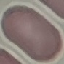
Summary:
  - Malaria status: uninfected
  - Stain: Giemsa
  - Preparation: thin smear
  - Capture: smartphone through the microscope eyepiece
  - Image type: cell patch, automatically extracted from a larger field of view and resized to 64 × 64 pixels